Identify the cell.
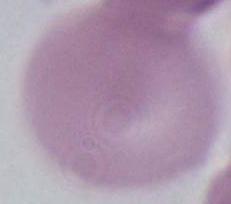

An erythrocyte.

Captured at 1000x magnification. Micrograph.